State the preparation type.
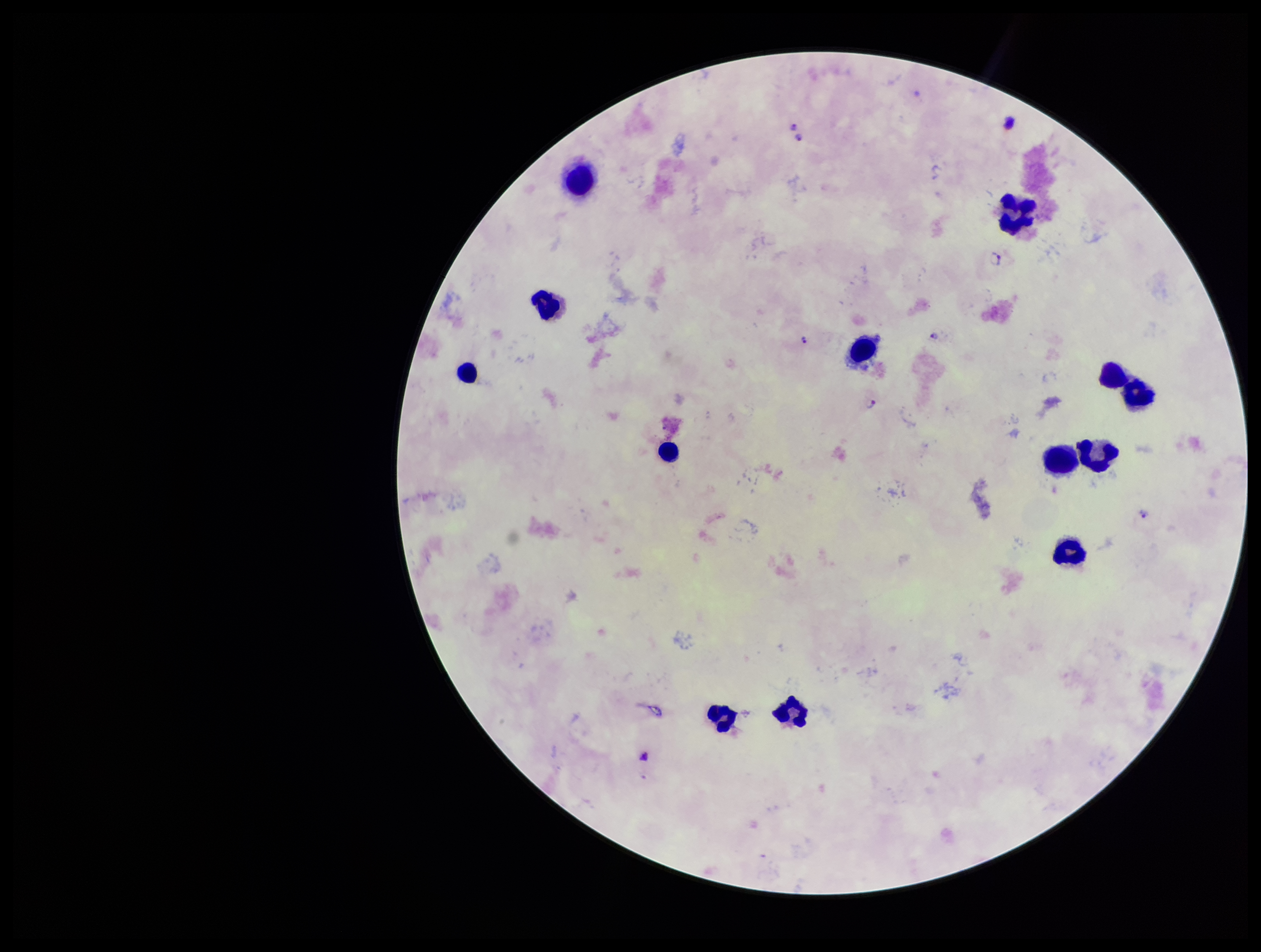
Thick.

parasite count = 7
stain = Giemsa
capture = smartphone photograph through the microscope eyepiece
leukocyte count = 13
field of view = one from this slide
image size = 1261×952 pixels
species reported for this patient = Plasmodium falciparum
Plasmodium parasites = detected
patient malaria status = positive